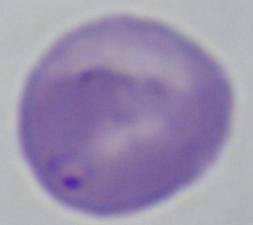
Summary:
  - Identification: Babesia
  - Modality: photomicrograph
  - Magnification: 1000x